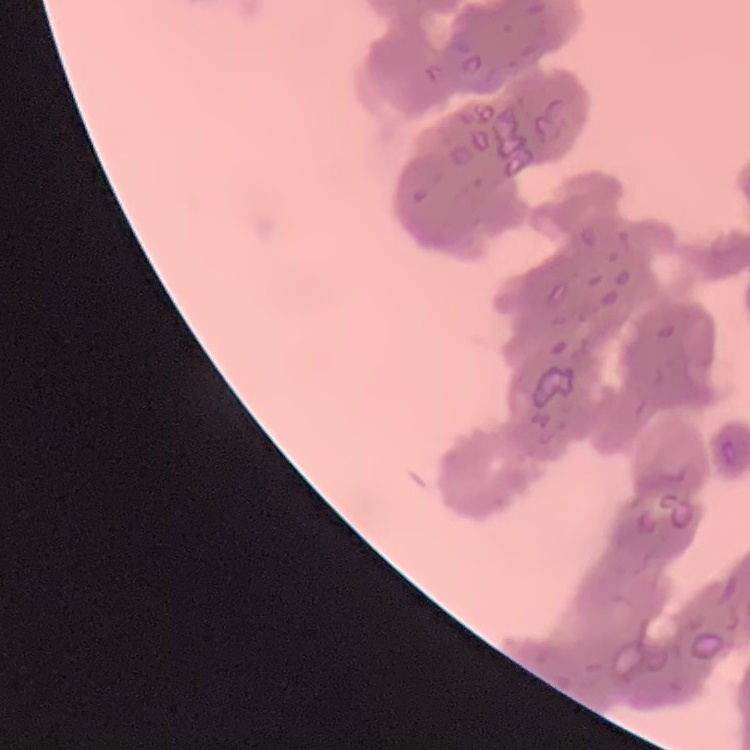

The red blood cells exhibit rouleaux formation. Stained with either Field's or Giemsa. Thin peripheral smear. Square crop of a larger photomicrograph.